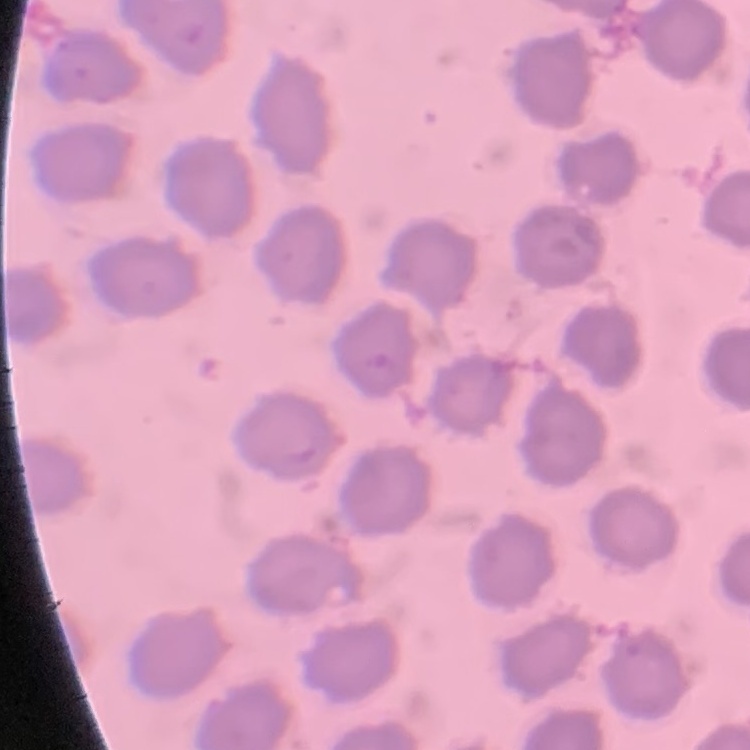
{
  "red_blood_cell_morphology": "no rouleaux formation",
  "image_type": "square crop of a larger photomicrograph",
  "stain": "Field's or Giemsa",
  "preparation": "thin peripheral smear"
}